Classify this cell by malaria status.
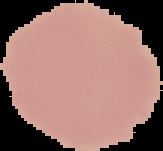
It is uninfected.

From a thin blood smear. Image is 163×151 pixels. Cell region segmented out of the field of view; the surrounding area is masked to black.